Identify the parasite.
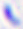
Toxoplasma gondii.

modality = photomicrograph
magnification = 400x